Report the malaria status of this cell.
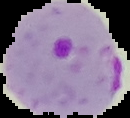

Parasitized.

Summary:
  - Image type: segmented cell region with the area outside set to black
  - Preparation: thin blood film
  - Image size: 130×118 pixels